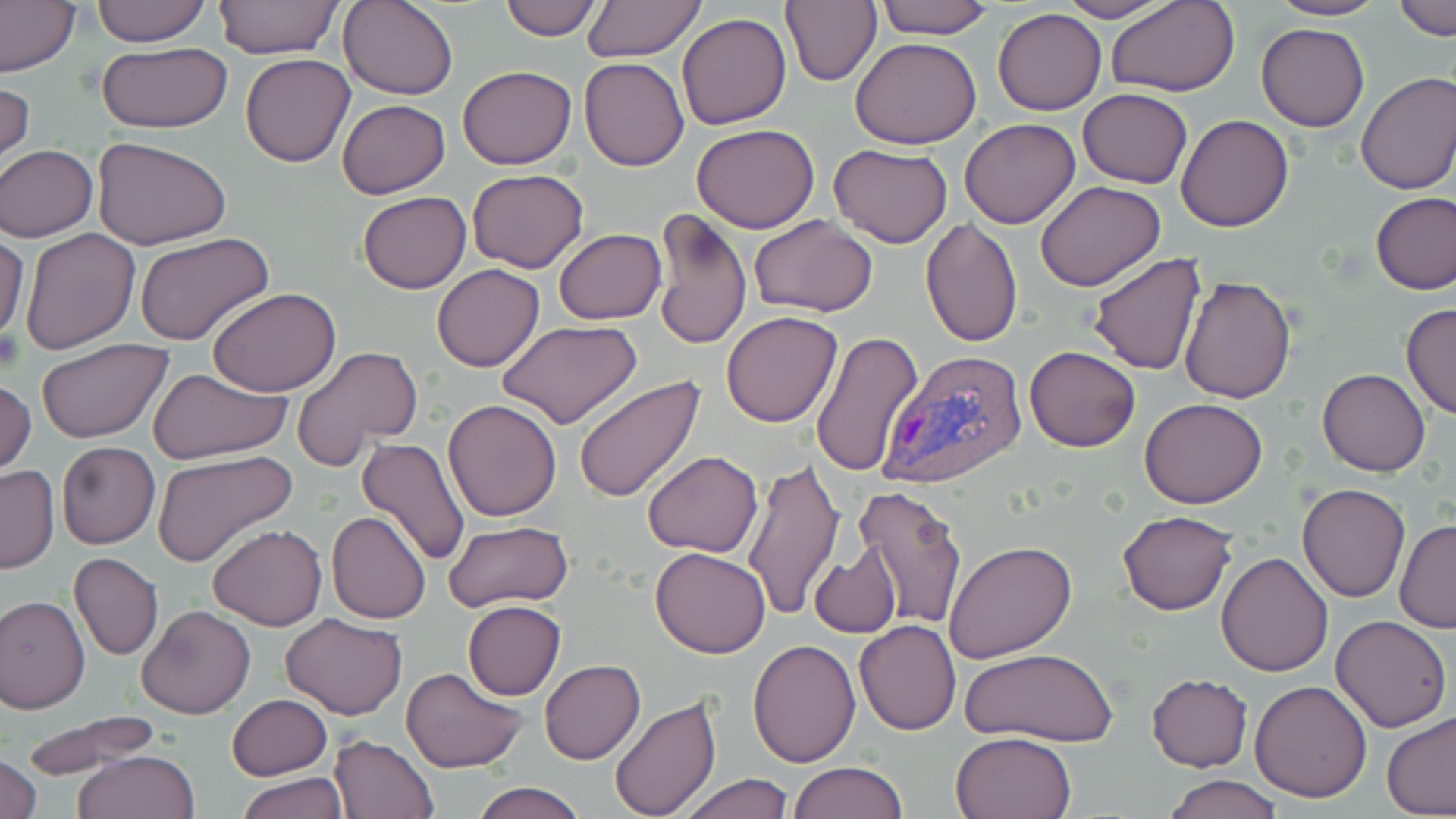

Approximate bounding boxes as named x1/y1/x2/y2 corners in pixels. Uninfected red blood cell locations: (x1=0, y1=0, x2=80, y2=78), (x1=90, y1=0, x2=211, y2=47), (x1=213, y1=0, x2=342, y2=60), (x1=338, y1=0, x2=459, y2=100), (x1=497, y1=0, x2=602, y2=41), (x1=581, y1=0, x2=707, y2=63), (x1=780, y1=0, x2=882, y2=88), (x1=873, y1=0, x2=995, y2=40), (x1=1053, y1=0, x2=1171, y2=23), (x1=1269, y1=0, x2=1387, y2=21), (x1=1105, y1=1, x2=1242, y2=97), (x1=1391, y1=1, x2=1455, y2=40), (x1=993, y1=7, x2=1108, y2=115), (x1=677, y1=12, x2=791, y2=130), (x1=1257, y1=23, x2=1370, y2=131), (x1=851, y1=37, x2=982, y2=149), (x1=96, y1=42, x2=232, y2=132), (x1=240, y1=53, x2=355, y2=166), (x1=578, y1=57, x2=689, y2=171), (x1=457, y1=65, x2=577, y2=168), (x1=1355, y1=71, x2=1456, y2=196), (x1=0, y1=79, x2=35, y2=172), (x1=1079, y1=89, x2=1192, y2=187), (x1=337, y1=99, x2=450, y2=199), (x1=1177, y1=114, x2=1294, y2=233), (x1=960, y1=118, x2=1080, y2=229), (x1=692, y1=124, x2=821, y2=233), (x1=94, y1=136, x2=230, y2=249), (x1=829, y1=143, x2=952, y2=247), (x1=0, y1=144, x2=98, y2=240), (x1=466, y1=169, x2=589, y2=273), (x1=1035, y1=179, x2=1166, y2=291), (x1=356, y1=192, x2=471, y2=293), (x1=1371, y1=192, x2=1456, y2=295), (x1=652, y1=207, x2=752, y2=351), (x1=749, y1=216, x2=877, y2=316), (x1=920, y1=218, x2=1023, y2=350), (x1=19, y1=228, x2=139, y2=353), (x1=554, y1=229, x2=665, y2=324), (x1=0, y1=233, x2=28, y2=342), (x1=135, y1=233, x2=274, y2=348), (x1=1085, y1=252, x2=1207, y2=376), (x1=431, y1=264, x2=545, y2=373), (x1=1178, y1=274, x2=1297, y2=403), (x1=207, y1=286, x2=342, y2=396), (x1=1401, y1=303, x2=1456, y2=420), (x1=720, y1=312, x2=843, y2=427), (x1=748, y1=312, x2=916, y2=445), (x1=498, y1=320, x2=643, y2=428), (x1=810, y1=332, x2=924, y2=477), (x1=36, y1=339, x2=172, y2=443), (x1=1024, y1=345, x2=1141, y2=452), (x1=292, y1=346, x2=421, y2=473), (x1=148, y1=367, x2=294, y2=467), (x1=1317, y1=368, x2=1431, y2=477), (x1=574, y1=372, x2=705, y2=500), (x1=0, y1=377, x2=35, y2=476), (x1=1139, y1=396, x2=1269, y2=509), (x1=443, y1=398, x2=563, y2=521), (x1=354, y1=437, x2=473, y2=569), (x1=57, y1=441, x2=160, y2=550), (x1=151, y1=449, x2=297, y2=566), (x1=642, y1=451, x2=763, y2=557), (x1=740, y1=459, x2=844, y2=622), (x1=0, y1=463, x2=59, y2=575), (x1=1296, y1=484, x2=1409, y2=602), (x1=853, y1=486, x2=968, y2=630), (x1=1116, y1=508, x2=1238, y2=616), (x1=326, y1=511, x2=432, y2=624), (x1=1395, y1=520, x2=1456, y2=633), (x1=442, y1=521, x2=573, y2=614), (x1=206, y1=525, x2=328, y2=631), (x1=943, y1=539, x2=1079, y2=664), (x1=810, y1=542, x2=903, y2=639), (x1=650, y1=547, x2=772, y2=658), (x1=1217, y1=551, x2=1333, y2=677), (x1=69, y1=552, x2=164, y2=661), (x1=1, y1=594, x2=90, y2=714), (x1=463, y1=601, x2=566, y2=700), (x1=138, y1=605, x2=256, y2=719), (x1=282, y1=612, x2=406, y2=719), (x1=1331, y1=615, x2=1453, y2=732), (x1=855, y1=620, x2=960, y2=735), (x1=748, y1=638, x2=860, y2=767), (x1=959, y1=648, x2=1118, y2=746), (x1=540, y1=659, x2=645, y2=765), (x1=400, y1=666, x2=528, y2=773), (x1=1148, y1=673, x2=1252, y2=771), (x1=1248, y1=679, x2=1374, y2=802), (x1=226, y1=694, x2=330, y2=781), (x1=608, y1=695, x2=721, y2=818), (x1=20, y1=711, x2=164, y2=778), (x1=1380, y1=711, x2=1456, y2=817), (x1=949, y1=731, x2=1078, y2=819), (x1=329, y1=733, x2=438, y2=818), (x1=74, y1=750, x2=201, y2=819), (x1=1, y1=752, x2=43, y2=819), (x1=788, y1=760, x2=908, y2=819), (x1=237, y1=774, x2=348, y2=818), (x1=679, y1=774, x2=795, y2=818), (x1=1165, y1=776, x2=1282, y2=818), (x1=469, y1=781, x2=586, y2=819). Plasmodium vivax-infected red blood cell locations: (x1=878, y1=347, x2=1032, y2=488). Slide-level diagnosis: Plasmodium vivax. Light microscopy. 1000x magnification. Single field of view. May-Grünwald-Giemsa-stained preparation. Image is 1456×819 pixels. Thin blood smear.